Comment on the morphology of the red blood cells.
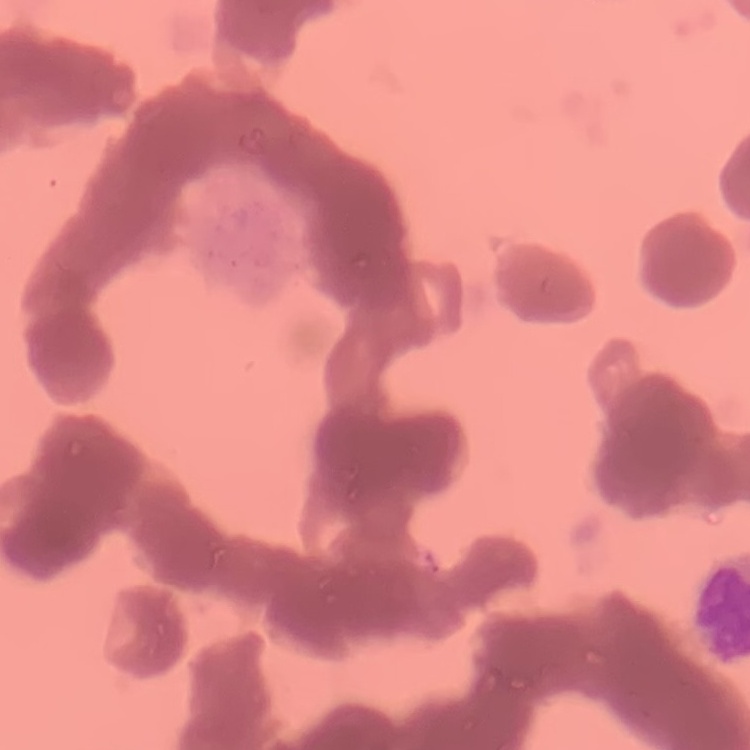
They show rouleaux formation.

Summary:
  - Stain: Field's or Giemsa
  - Preparation: thin blood film
  - Image type: square crop of a larger photomicrograph